Locate every blood parasite and identify its species.
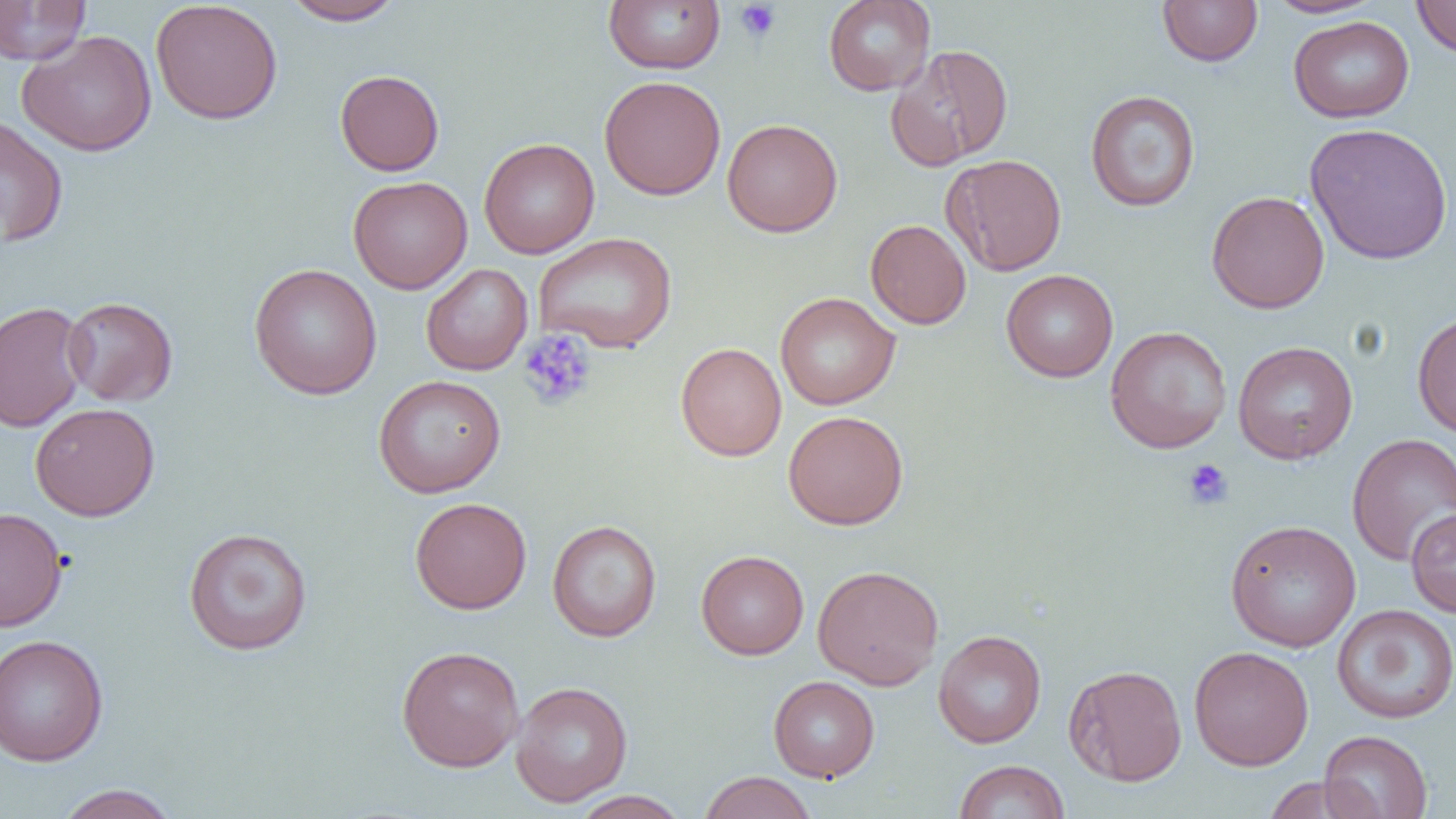
No blood parasites seen.

slide-level diagnosis = negative for blood parasites
magnification = 1000x
preparation = thin blood film
image size = 1456×819 pixels
field of view = single
uninfected red blood cell locations = approximate bounding boxes as [x1, y1, x2, y2] in pixels: [281, 0, 406, 25], [603, 0, 725, 74], [823, 0, 936, 96], [1264, 0, 1383, 18], [1411, 0, 1456, 58], [0, 1, 91, 65], [1157, 1, 1263, 67], [150, 2, 283, 125], [1288, 15, 1415, 123], [17, 30, 157, 157], [885, 44, 1014, 170], [335, 69, 445, 175], [599, 75, 726, 200], [1085, 90, 1201, 212], [0, 115, 69, 247], [722, 118, 842, 237], [1304, 122, 1454, 265], [479, 138, 599, 259], [943, 154, 1067, 276], [348, 175, 472, 294], [1206, 190, 1330, 314], [865, 219, 971, 329], [534, 232, 677, 353], [248, 263, 382, 399], [421, 263, 532, 375], [1000, 269, 1118, 382], [775, 291, 900, 410], [63, 296, 178, 406], [0, 301, 90, 432], [1412, 309, 1456, 438], [1104, 326, 1232, 453], [1233, 340, 1358, 464], [675, 342, 787, 461], [373, 375, 506, 497], [30, 402, 160, 521], [783, 410, 908, 529], [1347, 433, 1456, 566], [410, 496, 531, 614], [1, 507, 68, 631], [1406, 509, 1456, 617], [1225, 519, 1361, 652], [547, 520, 662, 642], [183, 526, 313, 655], [696, 549, 809, 660], [812, 564, 944, 690], [1332, 604, 1456, 724], [933, 630, 1047, 748], [0, 633, 109, 767], [396, 645, 524, 772], [1189, 646, 1314, 770], [1063, 663, 1187, 786], [768, 676, 880, 782], [510, 681, 633, 807], [1320, 730, 1433, 818], [953, 759, 1070, 819], [697, 771, 818, 819], [1262, 775, 1372, 818], [54, 783, 180, 819], [568, 790, 691, 819]
modality = optical microscopy
platelet locations = approximate bounding boxes as [x1, y1, x2, y2] in pixels: [734, 1, 782, 43], [519, 329, 597, 411], [1182, 458, 1234, 510]